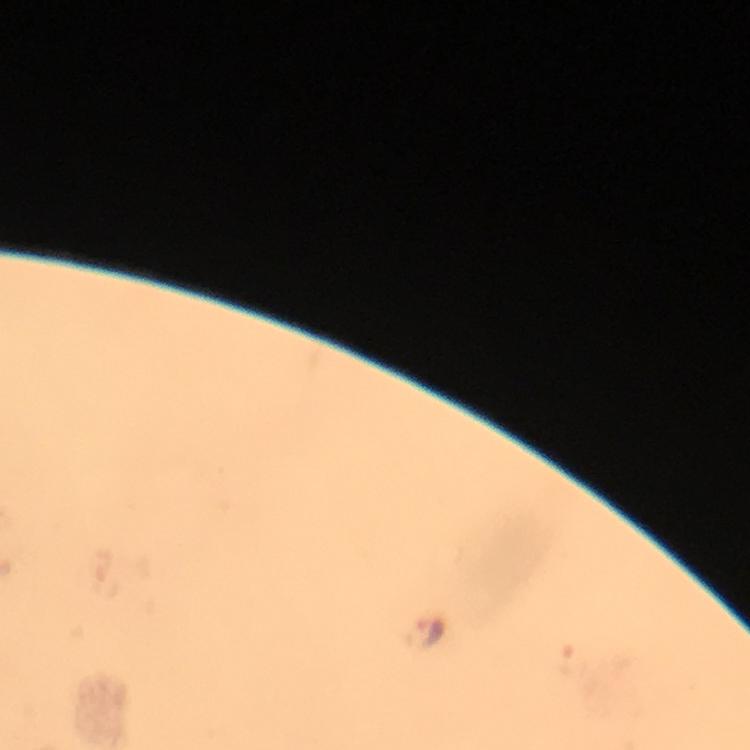
Approximate centers as {x, y} in pixels. Plasmodium parasite locations: {423, 632}. From a malaria diagnostic workup. Smartphone photograph taken through a microscope. 100x magnification. Image is 750×750 pixels. Thick blood smear. Giemsa-stained preparation. Immersion oil was used. Cropped region of a single field of view.